Identify the parasite.
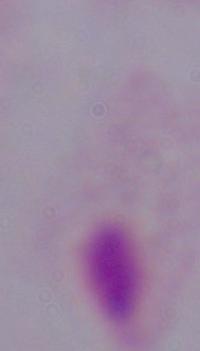

A trichomonad.

Photomicrograph. 1000x magnification.